Outline each Plasmodium falciparum-infected red blood cell.
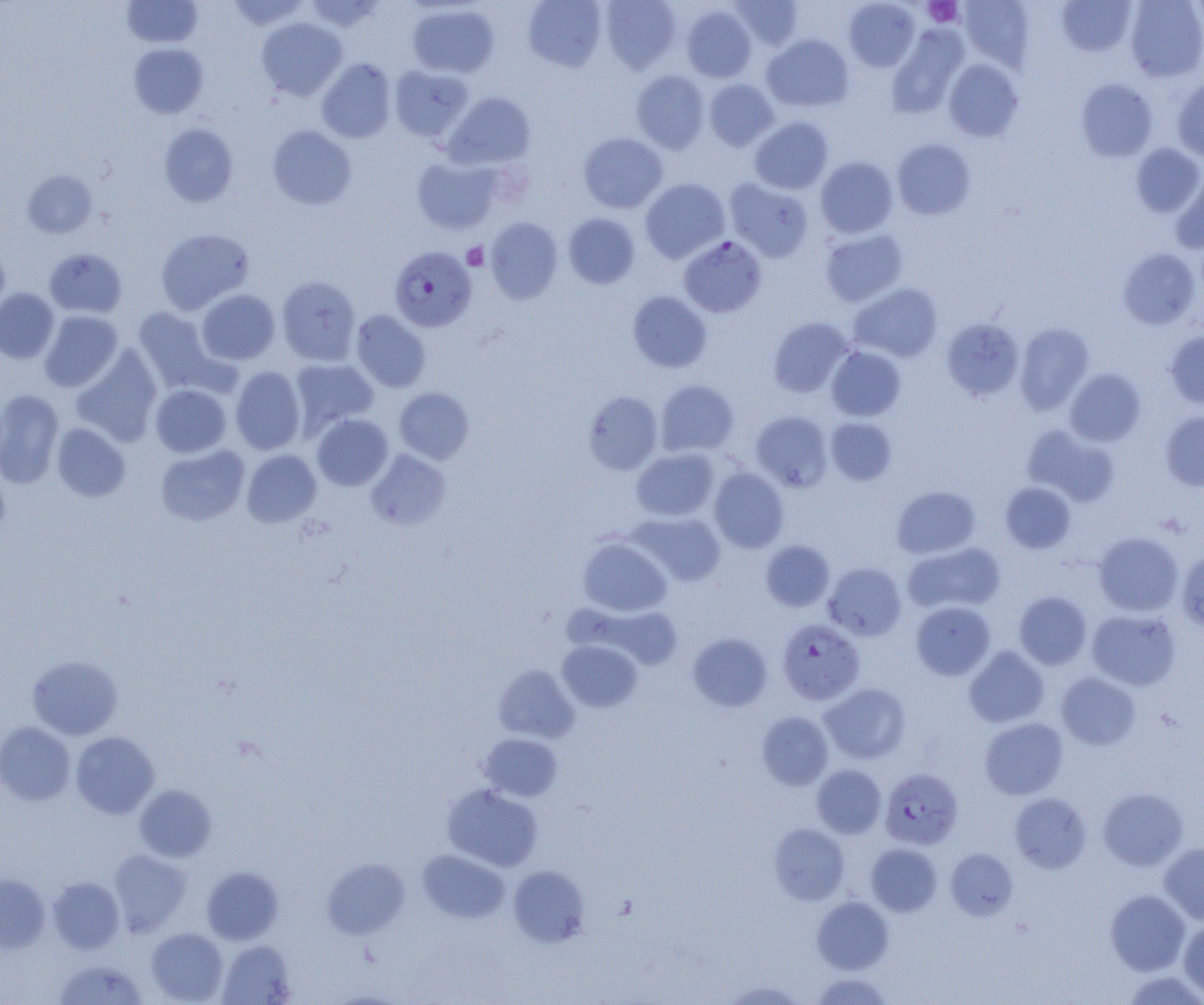

Approximate bounding boxes as (x1,y1)-(x2,y2) corner pairs in pixels.
Plasmodium falciparum-infected red blood cells: (679,237)-(767,318), (389,245)-(476,333), (777,620)-(865,705), (880,768)-(963,850).

{
  "slide_level_diagnosis": "Plasmodium falciparum",
  "field_of_view": "single",
  "uninfected_red_blood_cell_locations": "approximate bounding boxes as (x1,y1)-(x2,y2) corner pairs in pixels: (121,0)-(203,48), (226,0)-(311,31), (303,0)-(386,32), (523,0)-(607,71), (600,0)-(681,73), (729,0)-(803,51), (959,0)-(1035,69), (1057,0)-(1137,56), (1124,0)-(1204,82), (844,1)-(920,71), (407,3)-(499,78), (681,5)-(757,82), (257,17)-(348,100), (887,25)-(969,118), (762,35)-(853,111), (128,43)-(208,118), (317,58)-(397,143), (944,59)-(1023,142), (389,65)-(474,142), (631,69)-(710,153), (704,78)-(779,151), (1172,78)-(1204,160), (1076,79)-(1157,161), (443,92)-(536,170), (749,117)-(833,194), (159,123)-(239,207), (267,124)-(357,210), (578,133)-(668,213), (892,139)-(975,220), (1131,143)-(1203,217), (411,156)-(503,234), (815,156)-(898,238), (1171,169)-(1204,254), (22,170)-(97,238), (640,178)-(729,263), (725,178)-(814,261), (562,213)-(640,289), (485,217)-(563,304), (155,228)-(254,314), (820,230)-(908,307), (0,244)-(10,317), (44,247)-(127,318), (1118,248)-(1201,329), (276,275)-(361,366), (849,283)-(942,362), (0,288)-(59,363), (196,289)-(280,365), (628,291)-(712,372), (133,307)-(219,392), (350,309)-(431,392), (39,310)-(123,392), (768,317)-(854,397), (941,318)-(1024,400), (1015,323)-(1094,414), (1165,330)-(1204,409), (826,346)-(906,421), (71,347)-(163,447), (290,358)-(379,435), (230,366)-(306,454), (1064,368)-(1146,446), (655,379)-(739,457), (150,384)-(231,458), (394,387)-(474,464), (0,389)-(65,488), (583,391)-(663,475), (1160,410)-(1204,491), (751,411)-(833,492), (312,414)-(393,491), (826,417)-(897,485), (51,422)-(130,502), (1023,425)-(1120,506), (155,444)-(250,526), (241,449)-(321,527), (631,449)-(719,521), (366,450)-(451,530), (709,468)-(788,552), (1000,482)-(1076,553), (892,486)-(981,558), (628,512)-(726,586), (1093,532)-(1183,616), (578,537)-(672,616), (760,540)-(835,612), (903,542)-(1005,615), (1176,549)-(1204,633), (823,562)-(906,640), (1014,591)-(1091,670), (910,601)-(996,680), (579,603)-(684,671), (1086,609)-(1181,690), (688,633)-(772,712), (557,640)-(642,712), (964,646)-(1049,728), (27,655)-(123,739), (494,665)-(579,743), (1056,672)-(1141,750), (820,683)-(911,764), (756,711)-(834,790), (979,717)-(1068,799), (0,721)-(75,806), (71,731)-(159,818), (479,733)-(563,802), (811,764)-(886,838), (442,784)-(543,871), (134,785)-(216,862), (1098,787)-(1188,871), (1009,792)-(1091,873), (769,824)-(849,904), (865,843)-(942,917), (1159,843)-(1204,924), (945,848)-(1018,920), (108,849)-(191,936), (417,849)-(509,924), (322,857)-(410,939), (508,865)-(590,947), (201,866)-(283,944), (0,874)-(50,953), (47,876)-(124,954), (1105,889)-(1190,975), (812,896)-(894,974), (1178,919)-(1204,999), (145,927)-(228,1004), (217,939)-(296,1004), (53,958)-(148,1005), (1121,971)-(1204,1004), (811,972)-(894,1005), (722,979)-(806,1004)",
  "preparation": "thin blood smear",
  "magnification": "1000x",
  "image_size": "1204×1005 pixels",
  "platelet_locations": "approximate bounding boxes as (x1,y1)-(x2,y2) corner pairs in pixels: (923,0)-(962,26), (462,243)-(489,270)",
  "modality": "optical microscopy"
}